Assess this cell for malaria.
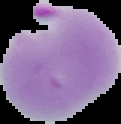

It is parasitized.

The area outside the segmented cell region is set to black. Image is 121×124 pixels. From a thin blood smear.